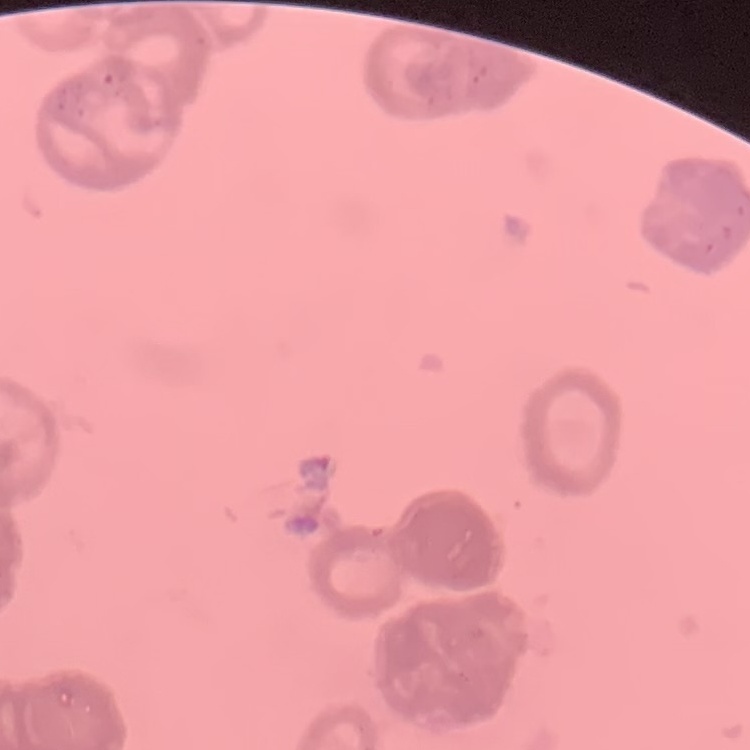
erythrocyte morphology = rouleaux formation
preparation = thin blood film
image type = one tile cut from a larger photomicrograph
stain = Field's or Giemsa